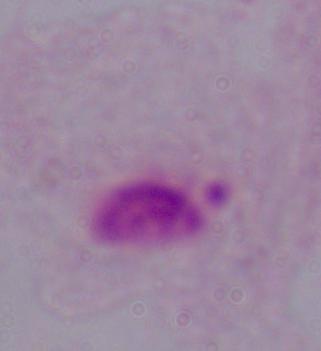
Summary:
  - Magnification: 1000x
  - Identification: trichomonad
  - Modality: micrograph